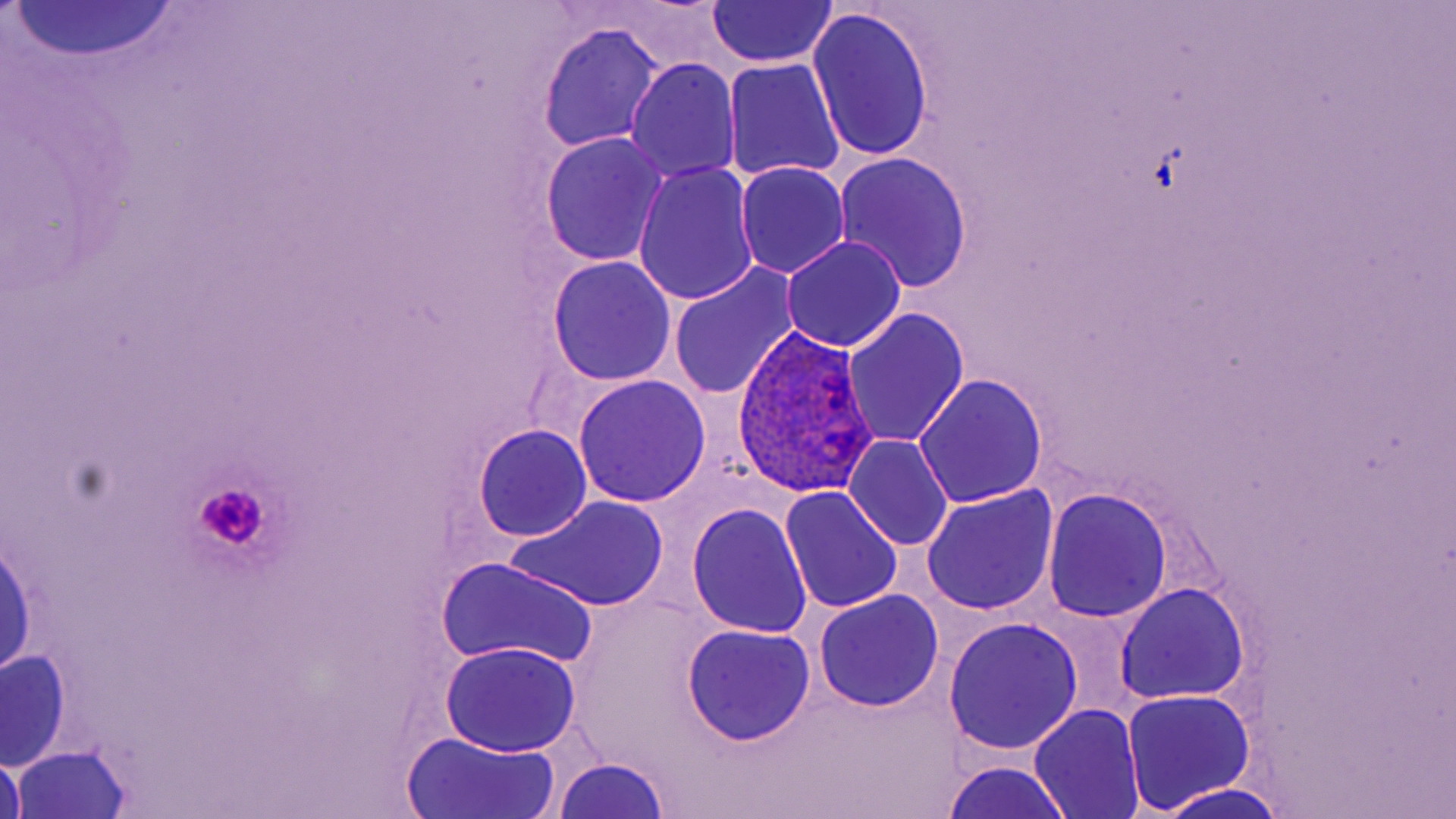
Summary:
  - Coordinate format: approximate bounding boxes as (x1,y1)-(x2,y2) corner pairs in pixels
  - Uninfected red blood cell locations: (7,2)-(182,63), (707,2)-(838,68), (808,7)-(936,164), (538,22)-(666,153), (624,57)-(741,184), (722,57)-(845,183), (539,131)-(671,266), (832,151)-(974,292), (735,160)-(849,278), (634,164)-(760,306), (782,234)-(907,352), (546,258)-(676,387), (667,262)-(800,401), (841,309)-(968,448), (572,374)-(712,507), (913,374)-(1048,509), (473,423)-(593,543), (844,435)-(954,550), (921,484)-(1060,616), (779,486)-(903,615), (1043,489)-(1173,623), (506,493)-(669,614), (687,504)-(813,639), (0,533)-(37,680), (435,556)-(598,672), (1115,582)-(1250,706), (813,591)-(943,712), (943,619)-(1081,755), (682,624)-(816,746), (440,641)-(583,757), (2,651)-(70,769), (1122,688)-(1256,813), (1029,703)-(1144,819), (403,729)-(562,819), (10,746)-(132,817), (0,750)-(29,819), (552,757)-(672,819), (940,760)-(1075,819), (1154,783)-(1292,819)
  - Platelet locations: (192,480)-(271,552)
  - Plasmodium ovale-infected red blood cell locations: (731,327)-(879,501)
  - Slide-level diagnosis: Plasmodium ovale
  - Modality: light microscopy
  - Image size: 1456×819 pixels
  - Magnification: 1000x
  - Preparation: thin blood smear
  - Stain: May-Grünwald-Giemsa
  - Field of view: single